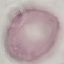
Malaria status: uninfected. Acquired by smartphone through the microscope eyepiece. Thin blood smear. Cell patch, automatically extracted from a larger field of view and resized to 64 × 64 pixels. Giemsa stain.